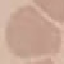

malaria status = uninfected
capture = smartphone camera at the microscope eyepiece
image type = automatically extracted cell patch, resized to 64 × 64 pixels
stain = Giemsa
preparation = thin smear